Comment on the morphology of the red blood cells.
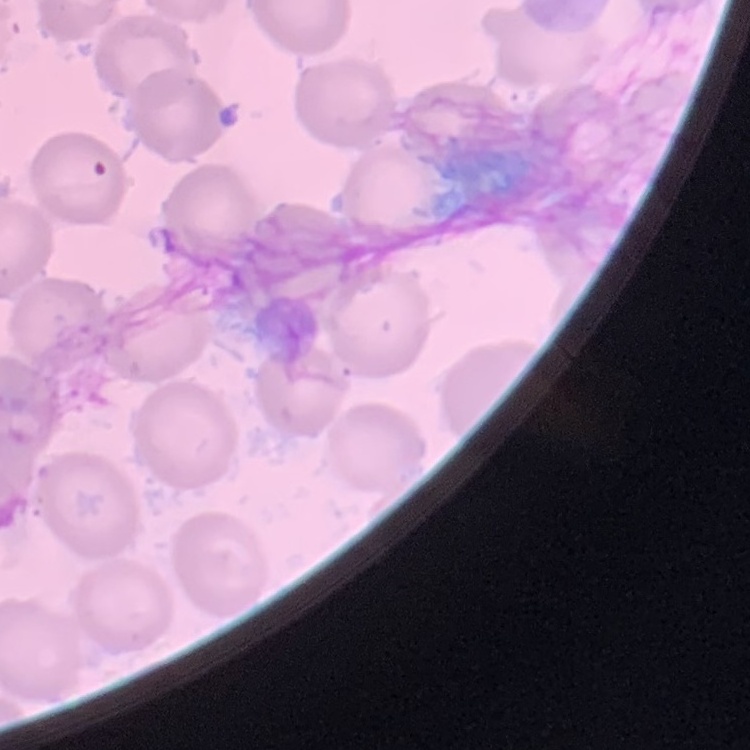

They show no rouleaux formation.

Stained with either Field's or Giemsa. Thin blood smear. One tile cut from a larger photomicrograph.